Identify the cell.
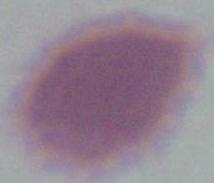

An erythrocyte.

Summary:
  - Modality: photomicrograph
  - Magnification: 1000x